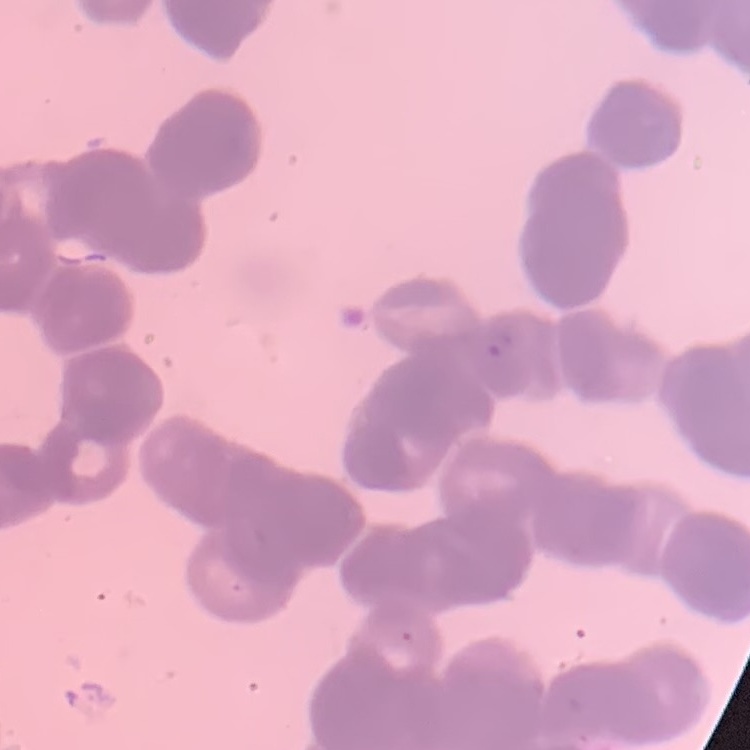
red blood cell morphology = rouleaux formation
image type = square crop of a larger photomicrograph
preparation = thin blood film
stain = Field's or Giemsa